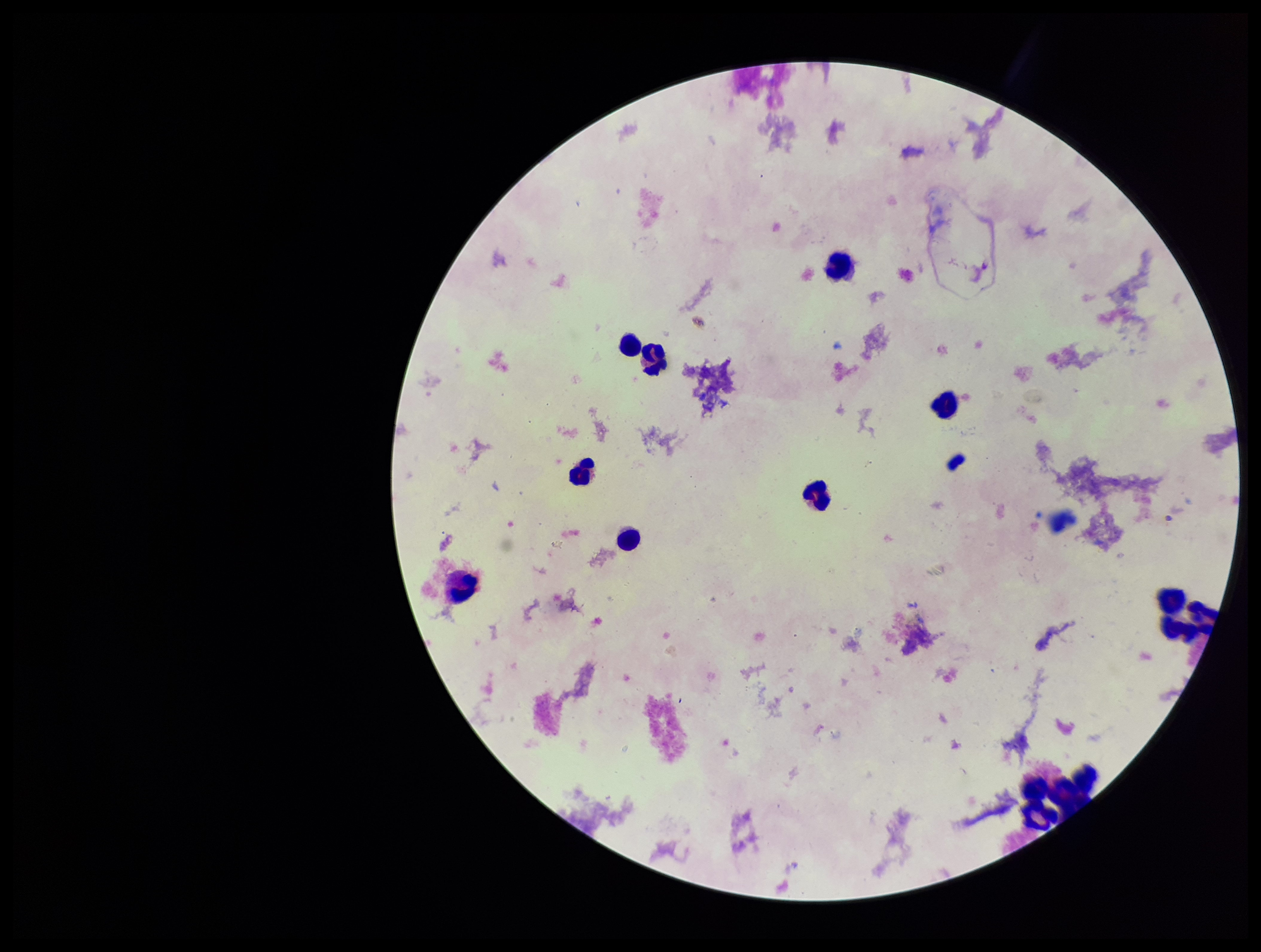

plasmodium_parasites: none detected
field_of_view: single
parasite_count: 0
capture: smartphone photograph through the microscope eyepiece
preparation: thick
patient_malaria_status: negative
image_size: 1261×952 pixels
leukocyte_count: 10
stain: Giemsa